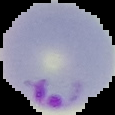
preparation = thin blood smear
malaria status = parasitized
image size = 115×115 pixels
image type = cell region segmented out of the field of view; surrounding area masked to black